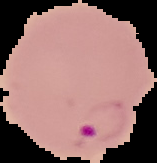
image_size: 157×163 pixels
preparation: thin blood smear
result: Plasmodium parasites identified
image_type: segmented cell region with the area outside set to black